Name the blood parasite species.
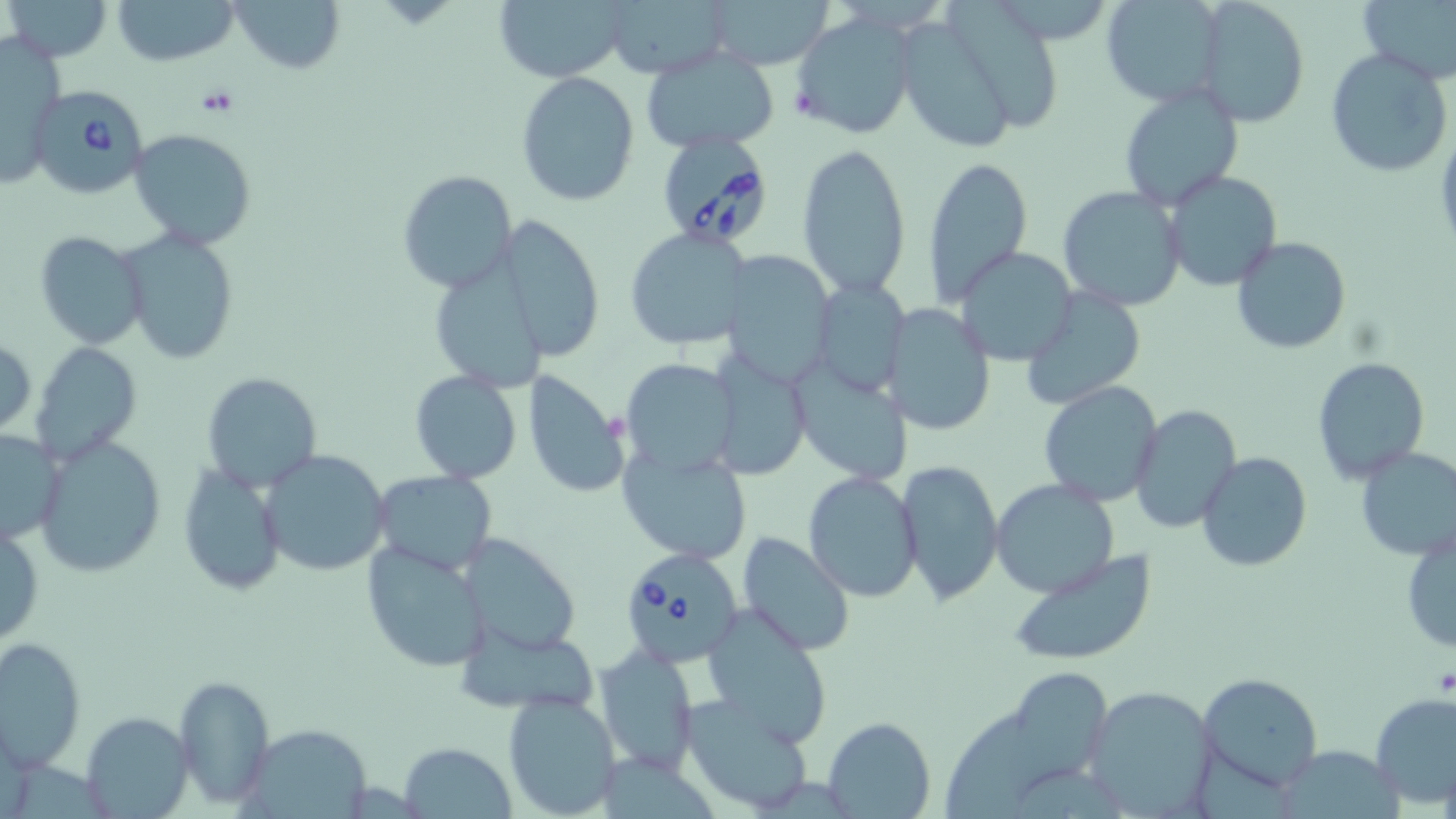

Babesia divergens.

Summary:
  - Coordinate format: approximate bounding boxes as (x1,y1)-(x2,y2) corner pairs in pixels
  - Babesia divergens-infected red blood cell locations: (30,84)-(148,199), (657,138)-(775,246), (617,544)-(745,666)
  - Platelet locations: (197,86)-(240,117)
  - Uninfected red blood cell locations: (5,0)-(112,62), (112,0)-(238,66), (228,0)-(347,75), (493,0)-(627,82), (604,0)-(733,79), (706,0)-(836,71), (1357,0)-(1456,85), (945,1)-(1063,137), (1099,1)-(1229,110), (1193,1)-(1310,127), (791,11)-(919,141), (904,22)-(1015,150), (1,31)-(66,187), (642,47)-(778,154), (1324,48)-(1454,178), (516,71)-(640,207), (1117,83)-(1245,211), (128,127)-(258,249), (796,139)-(912,300), (921,157)-(1034,308), (397,169)-(517,293), (1162,170)-(1282,291), (1057,186)-(1187,313), (496,216)-(606,362), (624,227)-(751,351), (116,228)-(241,365), (35,231)-(151,349), (1231,235)-(1354,355), (955,248)-(1078,365), (726,249)-(829,384), (436,252)-(548,391), (818,276)-(911,395), (1021,287)-(1145,409), (883,304)-(995,436), (0,334)-(36,439), (32,339)-(143,465), (706,353)-(814,481), (1312,356)-(1429,482), (625,359)-(739,483), (797,359)-(912,488), (410,370)-(523,483), (521,371)-(630,499), (202,373)-(322,492), (1039,380)-(1164,506), (1129,404)-(1243,536), (0,427)-(64,549), (33,435)-(166,577), (1354,445)-(1456,560), (618,446)-(752,564), (260,449)-(391,578), (1196,451)-(1312,573), (898,458)-(1004,606), (176,462)-(289,594), (371,470)-(495,577), (803,472)-(924,601), (990,480)-(1119,598), (1,518)-(44,650), (1402,527)-(1456,659), (737,530)-(854,659), (460,531)-(583,657), (361,541)-(488,670), (1006,549)-(1158,665), (701,604)-(834,745), (462,630)-(599,716), (0,636)-(85,772), (594,645)-(700,773), (1015,668)-(1110,790), (1197,672)-(1323,793), (172,674)-(274,808), (1085,684)-(1218,815), (503,691)-(623,818), (1370,694)-(1456,808), (681,695)-(816,815), (942,704)-(1048,819), (81,710)-(193,818), (823,716)-(936,818), (244,723)-(373,817), (399,742)-(518,819)
  - Preparation: thin blood film
  - Stain: May-Grünwald-Giemsa
  - Magnification: 1000x
  - Field of view: one of a larger specimen
  - Modality: optical microscopy
  - Image size: 1456×819 pixels